Find each cell and give its type.
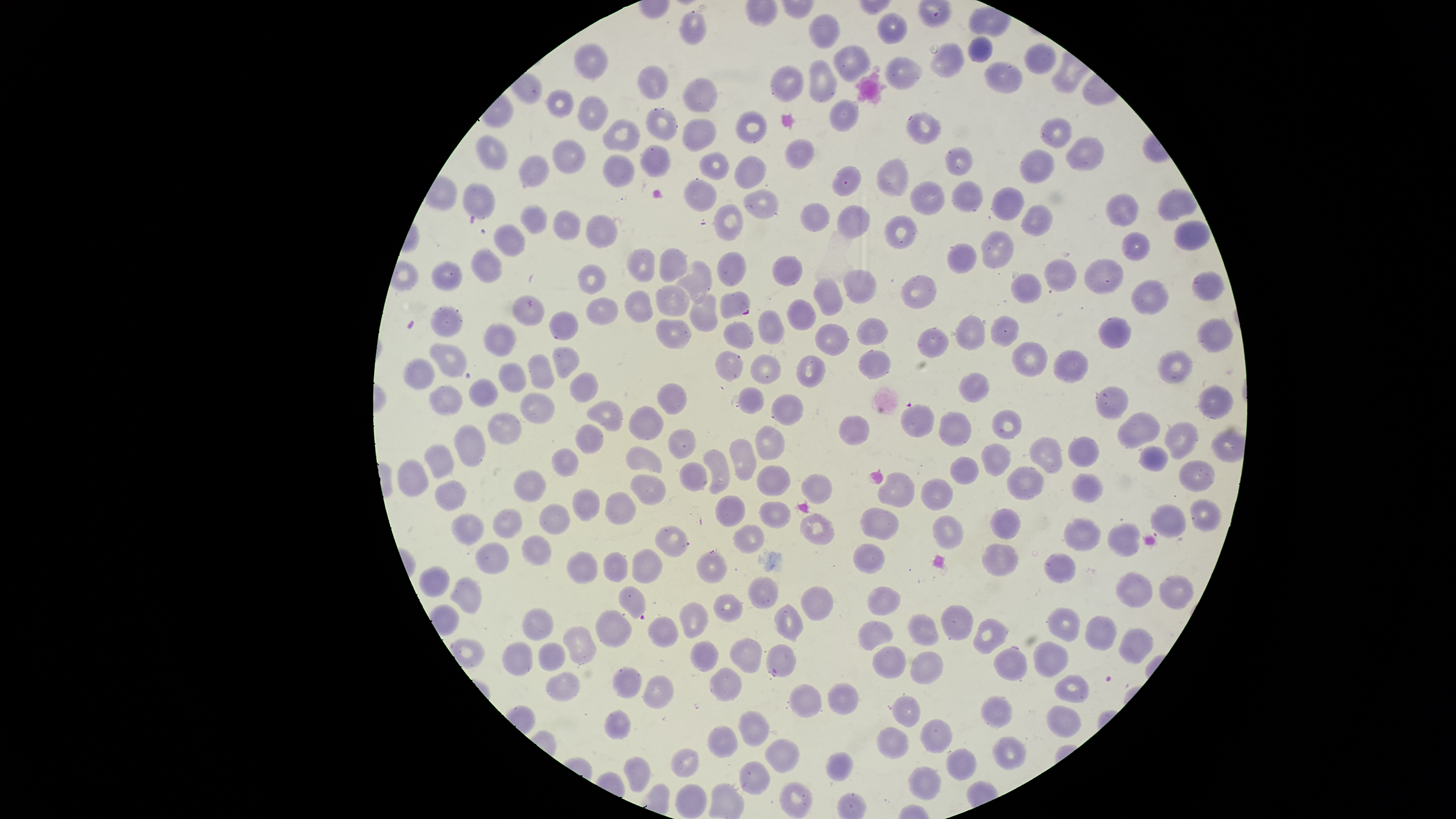

Approximate bounding boxes as (left, top, right, bottom) in pixels.
Parasitized red blood cells: (719, 290, 751, 319), (695, 549, 728, 583), (765, 644, 797, 680).
Uninfected red blood cells: (679, 10, 708, 46), (809, 13, 841, 50), (876, 13, 908, 44), (967, 36, 993, 64), (574, 41, 608, 81), (933, 41, 963, 77), (1025, 42, 1057, 74), (834, 43, 870, 81), (885, 56, 923, 89), (809, 60, 838, 102), (985, 62, 1024, 94), (771, 65, 804, 101), (638, 66, 668, 101), (683, 77, 718, 113), (548, 89, 575, 118), (579, 95, 609, 131), (830, 99, 860, 133), (646, 108, 678, 141), (736, 111, 767, 144), (907, 112, 942, 144), (1040, 117, 1073, 148), (601, 118, 641, 152), (682, 118, 716, 152), (476, 135, 509, 171), (1066, 136, 1104, 171), (785, 138, 814, 170), (553, 139, 586, 174), (640, 144, 671, 177), (946, 145, 974, 176), (699, 149, 729, 182), (1020, 150, 1054, 184), (518, 154, 550, 187), (603, 154, 635, 188), (735, 155, 766, 190), (877, 157, 910, 197), (833, 166, 862, 195), (684, 178, 718, 211), (910, 180, 945, 215), (952, 180, 984, 213), (463, 181, 495, 218), (993, 188, 1025, 221), (743, 189, 780, 218), (1159, 189, 1197, 221), (1106, 193, 1139, 226), (800, 202, 830, 232), (519, 203, 548, 233), (714, 204, 743, 241), (837, 204, 870, 239), (1021, 205, 1053, 236), (553, 211, 581, 241), (587, 213, 618, 248), (885, 216, 916, 249), (1175, 221, 1210, 251), (494, 223, 526, 257), (982, 230, 1015, 268), (1122, 232, 1151, 261), (947, 243, 978, 274), (626, 248, 655, 280), (659, 248, 687, 283), (471, 249, 503, 283), (718, 251, 747, 287), (772, 256, 803, 286), (1084, 258, 1124, 295), (1044, 260, 1076, 291), (430, 261, 463, 291), (678, 261, 712, 304), (578, 264, 605, 294), (844, 268, 877, 304), (1192, 271, 1225, 302), (1010, 273, 1042, 303), (901, 275, 936, 309), (813, 278, 844, 316), (1131, 280, 1170, 317), (657, 285, 690, 316), (626, 290, 653, 322), (690, 293, 718, 333), (512, 294, 544, 327), (586, 298, 620, 325), (786, 298, 817, 332), (430, 304, 463, 337), (757, 309, 785, 344), (549, 311, 580, 340), (956, 315, 985, 349), (991, 315, 1020, 347), (1098, 316, 1131, 349), (655, 317, 692, 350), (1197, 317, 1233, 353), (856, 318, 887, 345), (724, 320, 756, 350), (483, 322, 518, 357), (815, 323, 850, 356), (918, 327, 948, 358), (1010, 342, 1046, 377), (430, 344, 468, 377), (552, 347, 579, 379), (859, 348, 891, 379), (1158, 349, 1193, 384), (716, 350, 743, 380), (1054, 350, 1089, 382), (529, 354, 554, 389), (750, 354, 781, 385), (796, 355, 826, 387), (403, 357, 436, 390), (499, 362, 528, 395), (570, 372, 596, 403), (960, 372, 989, 404), (470, 379, 499, 407), (656, 382, 687, 415), (429, 385, 463, 415), (1199, 385, 1234, 420), (739, 386, 765, 415), (1096, 386, 1130, 419), (521, 392, 556, 425), (772, 394, 805, 426), (586, 399, 623, 431), (629, 405, 663, 440), (901, 405, 934, 438), (991, 409, 1022, 440), (939, 412, 971, 447), (1118, 412, 1159, 448), (487, 413, 520, 444), (839, 416, 870, 445), (1165, 422, 1198, 460), (576, 425, 604, 454), (755, 425, 784, 459), (454, 426, 484, 467), (667, 429, 695, 459), (1068, 436, 1100, 468), (729, 437, 757, 480), (1029, 438, 1063, 475), (424, 443, 454, 479), (982, 444, 1012, 475), (626, 446, 663, 474), (1140, 446, 1169, 471), (551, 448, 580, 478), (703, 449, 730, 495), (950, 456, 980, 485), (398, 459, 428, 496), (1179, 460, 1215, 492), (678, 461, 707, 491), (757, 465, 790, 497), (1007, 466, 1043, 500), (513, 470, 547, 501), (879, 471, 915, 507), (1072, 472, 1103, 503), (630, 473, 666, 506), (801, 474, 831, 504), (922, 476, 953, 512), (434, 479, 467, 510), (572, 487, 600, 522), (605, 492, 638, 523), (715, 495, 745, 528), (1189, 498, 1223, 532), (760, 501, 790, 529), (538, 504, 571, 536), (1151, 504, 1186, 539), (493, 508, 523, 539), (861, 508, 898, 540), (990, 509, 1021, 540), (454, 512, 483, 545), (801, 514, 834, 546), (932, 515, 964, 548), (1064, 519, 1102, 551), (1108, 523, 1141, 557), (734, 525, 765, 554), (656, 526, 688, 557), (521, 533, 552, 567), (475, 541, 510, 574), (853, 544, 884, 573), (983, 544, 1019, 576), (632, 549, 663, 585), (567, 551, 597, 584), (603, 551, 628, 582), (1043, 552, 1076, 583), (418, 566, 449, 595), (1115, 571, 1152, 608), (1159, 575, 1193, 609), (749, 576, 778, 608), (451, 578, 481, 614), (617, 585, 647, 618), (869, 586, 901, 615), (800, 587, 833, 621), (713, 594, 744, 623), (680, 601, 709, 638), (774, 604, 803, 642), (942, 605, 973, 640), (595, 608, 632, 647), (1046, 608, 1081, 642), (523, 610, 553, 640), (648, 614, 678, 646), (908, 614, 940, 647), (1085, 615, 1116, 652), (973, 618, 1007, 654), (858, 621, 894, 650), (563, 625, 597, 664), (1121, 629, 1153, 664), (730, 635, 762, 673), (691, 640, 718, 672), (536, 641, 565, 670), (501, 642, 532, 676), (1034, 642, 1069, 677), (873, 646, 906, 680), (994, 648, 1028, 681), (912, 651, 942, 684), (613, 666, 643, 698), (710, 668, 741, 701), (547, 670, 581, 702), (645, 675, 673, 709), (1054, 675, 1089, 703), (826, 682, 859, 715), (788, 684, 822, 718), (982, 695, 1012, 728), (893, 696, 920, 727), (1047, 706, 1082, 738), (606, 709, 631, 738), (739, 711, 768, 747), (921, 720, 953, 752), (708, 727, 738, 758), (878, 728, 910, 758), (993, 736, 1025, 770), (766, 740, 798, 774), (670, 749, 698, 778), (948, 749, 976, 781), (825, 751, 854, 782), (624, 756, 650, 791), (739, 763, 770, 794), (906, 766, 942, 799), (780, 781, 812, 816), (675, 782, 707, 817).
No white blood cells identified.

Giemsa-stained preparation. Photographed with a smartphone camera through the microscope eyepiece. One field of view of the specimen. Species: Plasmodium falciparum. Thin blood smear. Image is 1456×819 pixels. The visible region is circular.